Report the malaria status of this cell.
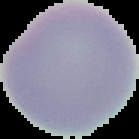
Uninfected.

Summary:
  - Preparation: thin blood film
  - Image type: segmented cell region with the area outside set to black
  - Image size: 139×139 pixels